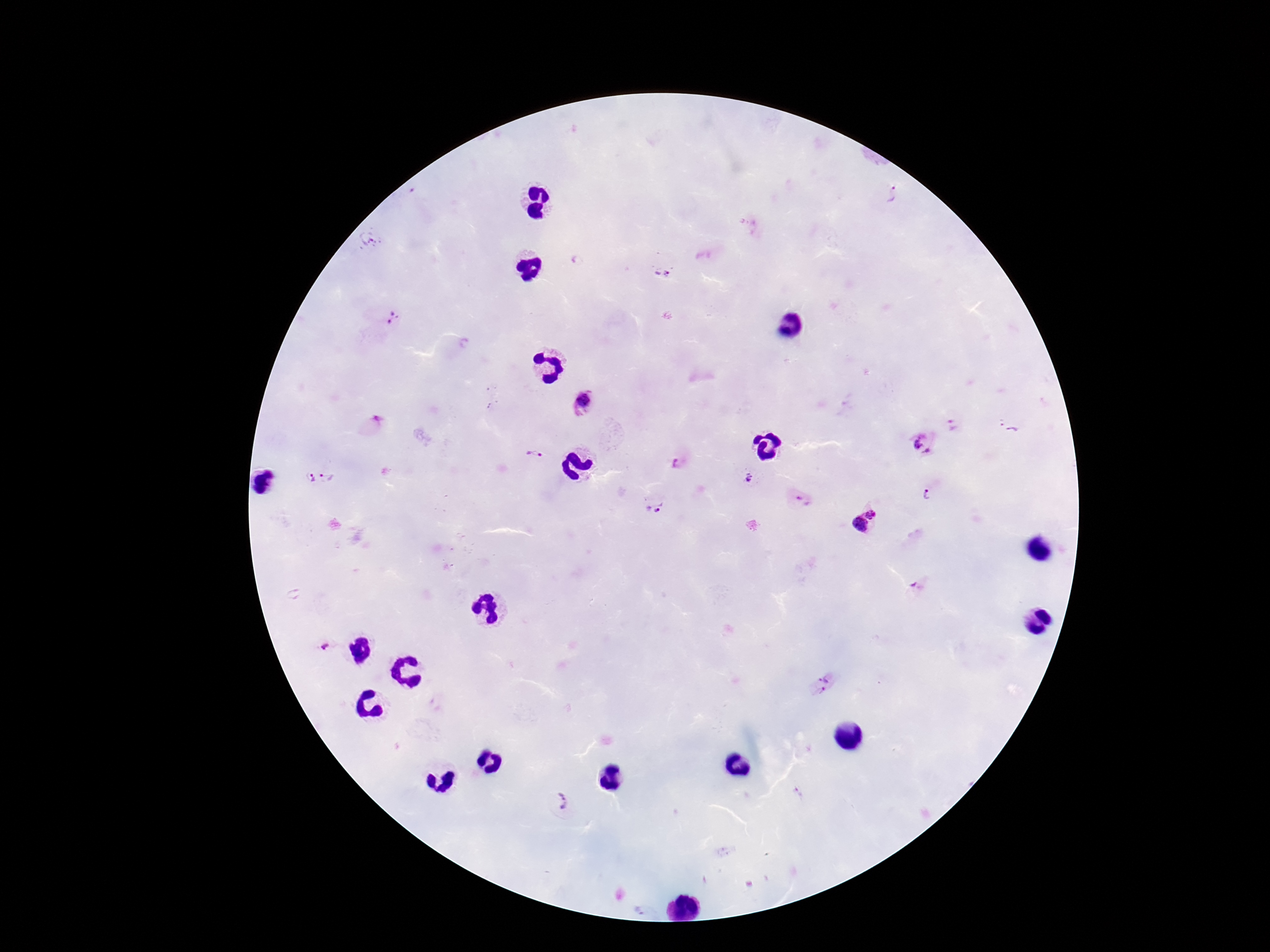

Approximate centers as (x, y) in pixels.
Summary:
  - Plasmodium parasite locations: (892, 196), (366, 240), (662, 273), (393, 318), (582, 402), (375, 424), (955, 425), (1010, 426), (923, 442), (533, 457), (679, 465), (328, 476), (311, 479), (749, 479), (929, 495), (803, 500), (655, 508), (873, 513), (858, 525), (918, 586), (321, 647), (827, 676), (819, 693), (798, 793), (561, 803), (639, 910)
  - Image size: 1270×952 pixels
  - Stain: Giemsa
  - Capture: smartphone camera through the microscope eyepiece
  - Preparation: thick peripheral-blood smear
  - Patient malaria status: infected
  - Magnification: 100x
  - Field of view: one from this slide